Name the parasite shown.
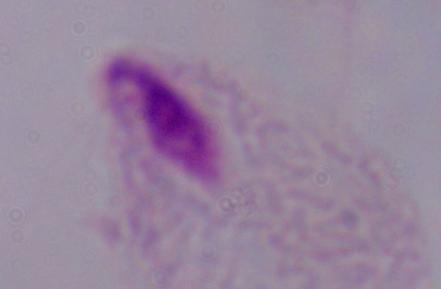

This is a trichomonad.

magnification = 1000x
modality = photomicrograph